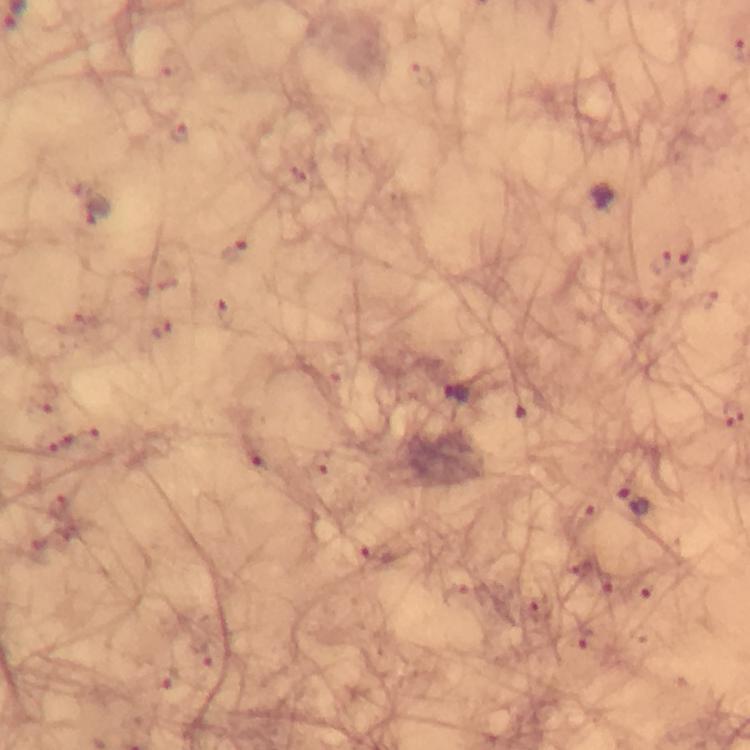
Approximate centers as {x, y} in pixels. Plasmodium parasite locations: {600, 198}, {662, 263}, {457, 393}, {733, 416}, {631, 500}. Cropped region of a single field of view. Giemsa-stained preparation. 100x magnification. Thick smear. Immersion oil was used. From a diagnostic examination for malaria. Image is 750×750 pixels. Photographed through the microscope with a smartphone camera.